Locate every malaria parasite.
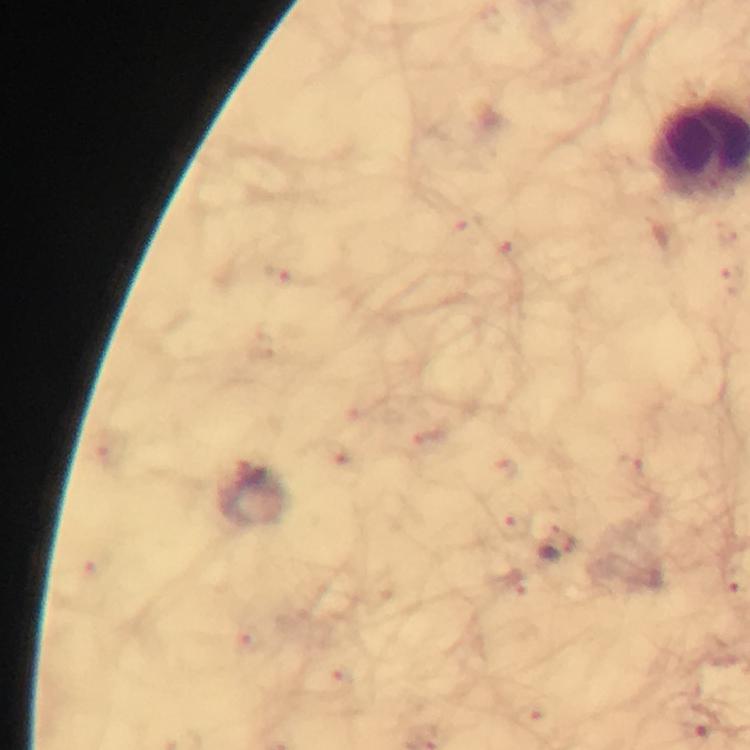

Approximate centers as (x, y) in pixels.
Malaria parasites: (557, 549).

Thick blood film. Giemsa-stained preparation. Photographed with a smartphone mounted on the microscope. 100x magnification. Cropped region of a single field of view. From a malaria diagnostic workup. Immersion oil was used. Image is 750×750 pixels.